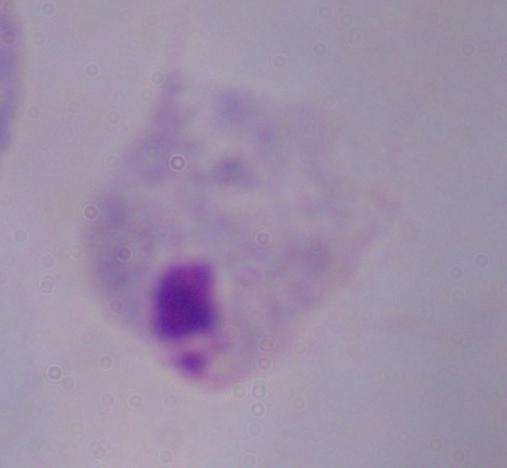
{
  "magnification": "1000x",
  "modality": "micrograph",
  "identification": "trichomonad"
}